Evaluate for Plasmodium parasites.
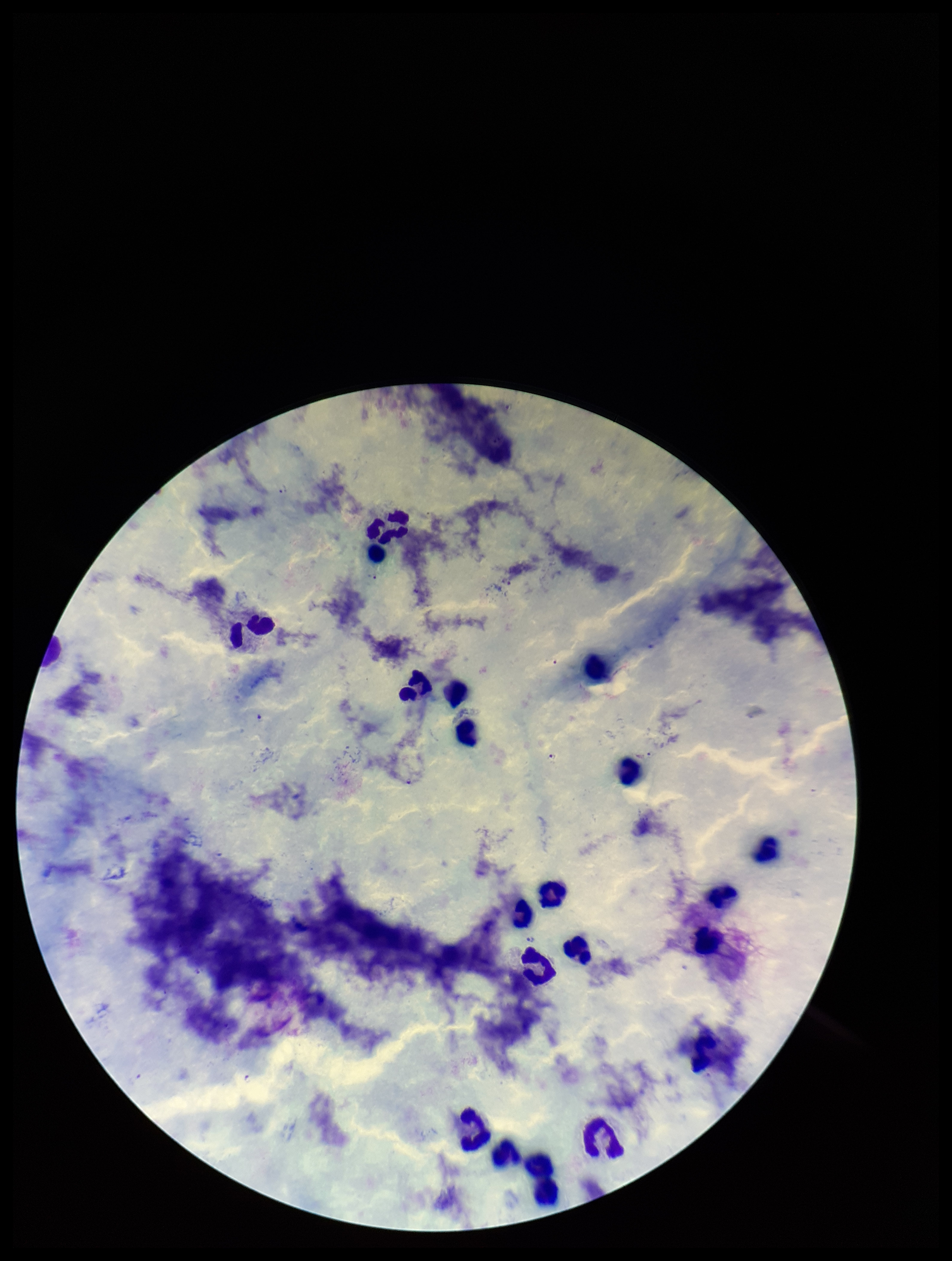

Seen.

Parasite count: 6. Preparation: thick smear. Image is 952×1261 pixels. Leukocyte count: 20. Species reported for this patient: Plasmodium falciparum. Smartphone photograph taken through the eyepiece of a microscope. Stained with Giemsa. One field from this slide. Patient malaria status: positive.